Give the extent of all Plasmodium malariae-infected red blood cells.
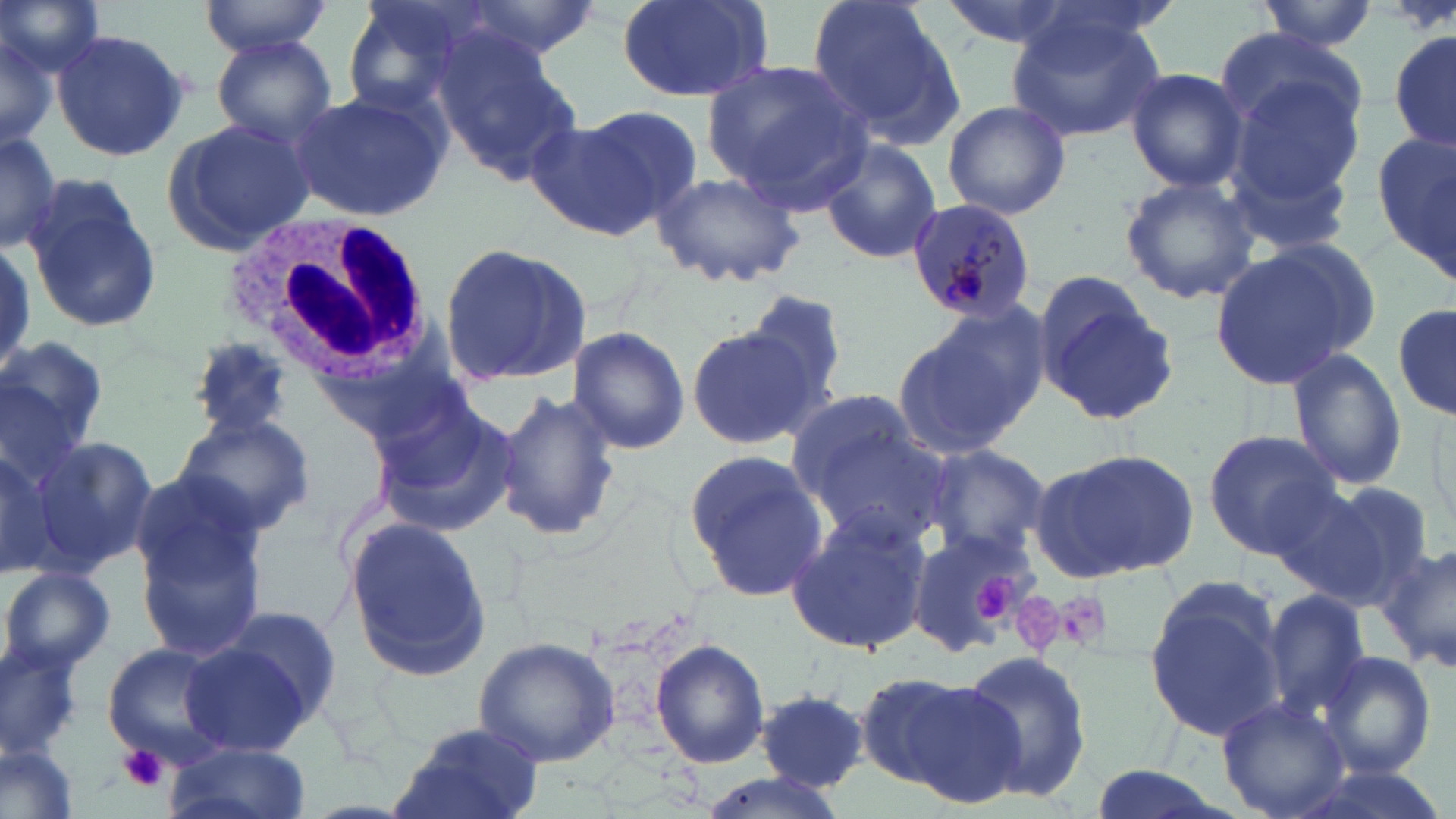

Approximate bounding boxes as [x1, y1, x2, y2] in pixels.
Plasmodium malariae-infected red blood cells: [907, 200, 1037, 325].

Summary:
  - White blood cell locations: [221, 214, 431, 392]
  - Platelet locations: [964, 571, 1023, 629], [1056, 592, 1114, 650], [1020, 595, 1065, 651], [120, 744, 167, 792]
  - Uninfected red blood cell locations: [0, 0, 107, 77], [200, 0, 334, 56], [340, 0, 495, 115], [452, 0, 605, 62], [616, 0, 772, 101], [807, 0, 962, 144], [935, 0, 1085, 50], [1257, 1, 1382, 51], [1005, 8, 1168, 142], [0, 24, 59, 151], [1388, 27, 1456, 157], [50, 28, 191, 162], [1216, 30, 1364, 150], [211, 35, 336, 147], [432, 35, 579, 183], [704, 63, 872, 206], [1126, 68, 1248, 192], [1235, 80, 1366, 201], [285, 85, 452, 222], [943, 99, 1071, 220], [573, 104, 704, 220], [165, 114, 315, 254], [524, 117, 665, 239], [1224, 121, 1358, 254], [0, 129, 63, 253], [1376, 133, 1455, 275], [818, 136, 942, 265], [646, 167, 808, 292], [23, 171, 163, 334], [1119, 175, 1258, 306], [438, 240, 592, 390], [0, 242, 34, 377], [1208, 242, 1369, 389], [1032, 275, 1177, 426], [743, 288, 856, 408], [1393, 299, 1454, 421], [894, 310, 1041, 460], [685, 324, 817, 451], [566, 326, 691, 456], [185, 333, 299, 441], [0, 335, 109, 465], [1288, 346, 1406, 491], [784, 387, 921, 502], [496, 388, 623, 545], [371, 391, 520, 535], [1426, 403, 1455, 539], [173, 411, 316, 536], [1202, 429, 1342, 557], [806, 430, 954, 550], [30, 434, 157, 577], [923, 443, 1051, 559], [681, 449, 831, 602], [1032, 450, 1199, 580], [131, 477, 266, 657], [1263, 479, 1397, 606], [1324, 481, 1437, 596], [784, 511, 930, 655], [343, 513, 491, 683], [906, 527, 1037, 655], [1379, 540, 1456, 676], [2, 564, 115, 677], [1144, 579, 1289, 742], [1261, 588, 1373, 722], [216, 606, 347, 729], [472, 636, 622, 768], [179, 637, 316, 757], [651, 639, 770, 768], [103, 643, 225, 764], [0, 644, 83, 760], [957, 650, 1094, 803], [1315, 651, 1437, 778], [864, 671, 1025, 803], [757, 690, 869, 790], [1217, 697, 1352, 819], [390, 724, 547, 819], [1, 740, 80, 819], [165, 744, 313, 819], [691, 770, 852, 819]
  - Slide-level diagnosis: Plasmodium malariae
  - Image size: 1456×819 pixels
  - Magnification: 1000x
  - Preparation: thin blood smear
  - Field of view: one of a larger specimen
  - Stain: May-Grünwald-Giemsa
  - Modality: light microscopy